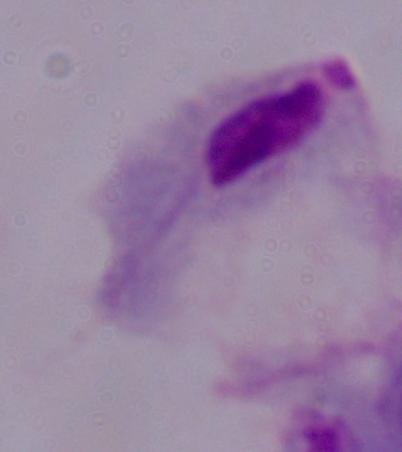

{
  "modality": "photomicrograph",
  "magnification": "1000x",
  "identification": "trichomonad"
}